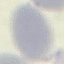
Summary:
  - Result: no malaria parasites seen
  - Preparation: thin smear
  - Stain: Giemsa
  - Capture: smartphone through the microscope eyepiece
  - Image type: cell patch, automatically extracted from a larger field of view and resized to 64 × 64 pixels